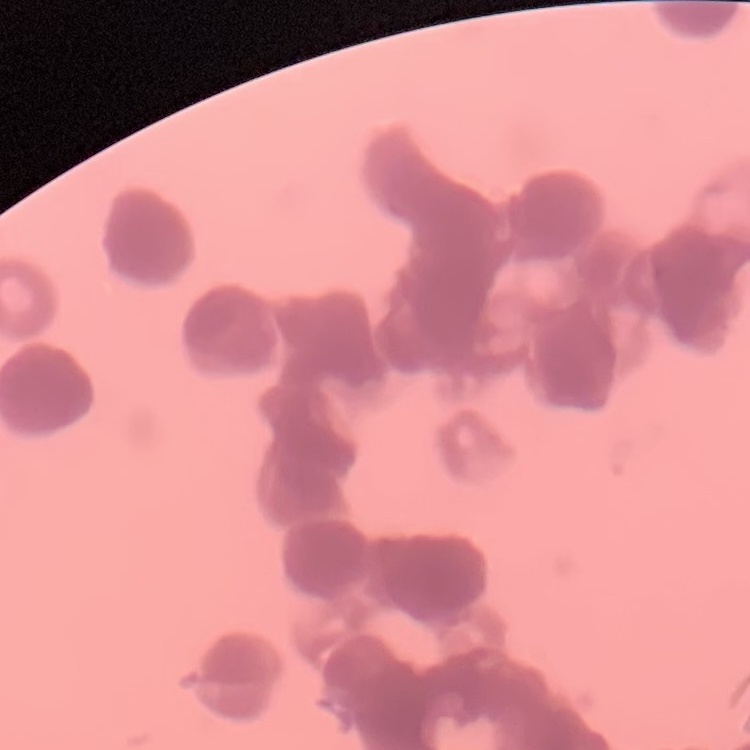

The erythrocytes exhibit rouleaux formation. Thin peripheral smear. Stained with either Field's or Giemsa. One tile cut from a larger photomicrograph.